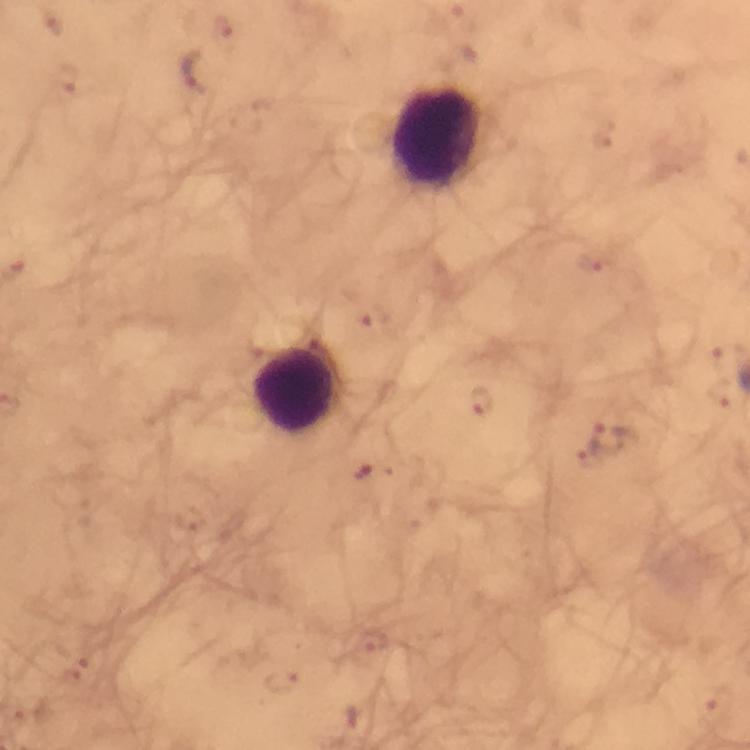
capture = smartphone mounted on the microscope
preparation = thick blood smear
Plasmodium parasite locations = approximate centers as {x, y} in pixels: {54, 22}, {223, 27}, {197, 72}, {68, 79}, {604, 136}, {588, 262}, {370, 319}, {725, 355}, {719, 391}, {480, 401}, {612, 441}, {584, 459}, {363, 472}, {189, 518}, {71, 666}, {282, 683}, {714, 704}
image size = 750×750 pixels
stain = Giemsa
context = from a diagnostic examination for malaria
cropped from = one field of view
leukocyte locations = approximate centers as {x, y} in pixels: {435, 138}, {295, 392}
immersion oil = used
magnification = 100x